Describe the morphology of the red blood cells.
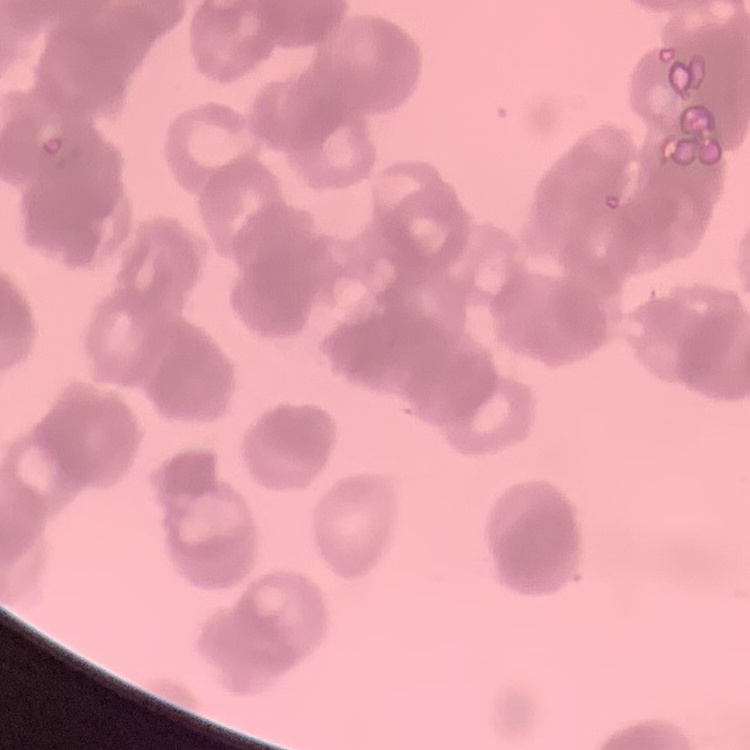
Rouleaux formation.

Summary:
  - Preparation: thin peripheral smear
  - Stain: Field's or Giemsa
  - Image type: one tile cut from a larger photomicrograph